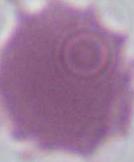

{
  "identification": "erythrocyte",
  "modality": "photomicrograph",
  "magnification": "1000x"
}